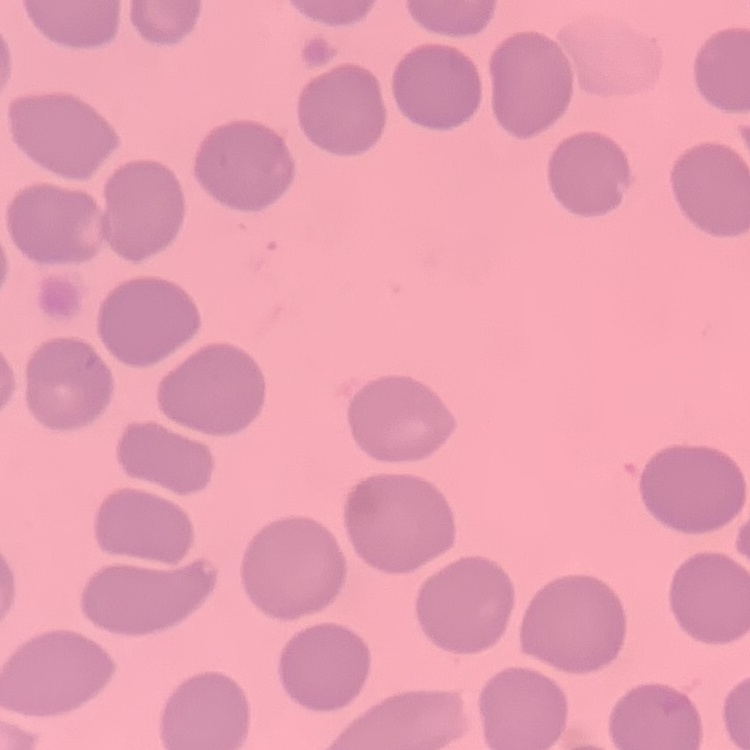
erythrocyte morphology = no rouleaux formation
preparation = thin peripheral smear
stain = Field's or Giemsa
image type = square crop of a larger photomicrograph